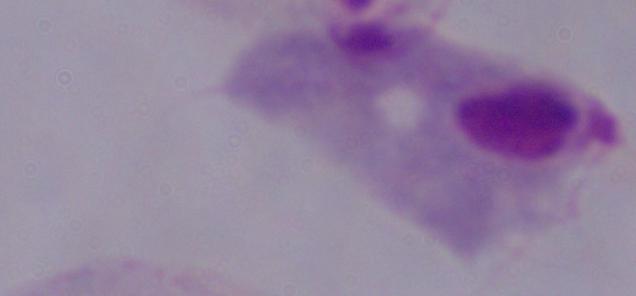
A trichomonad is shown. Micrograph. Captured at 1000x magnification.